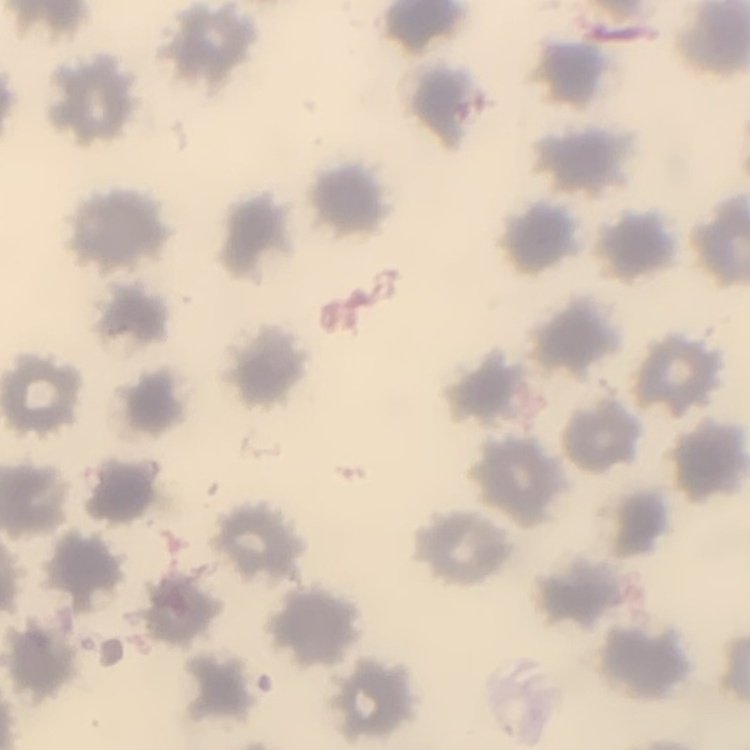

erythrocyte morphology = no rouleaux formation
image type = one tile cut from a larger photomicrograph
stain = Field's or Giemsa
preparation = thin peripheral smear